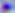

modality: photomicrograph
magnification: 400x
identification: Toxoplasma gondii